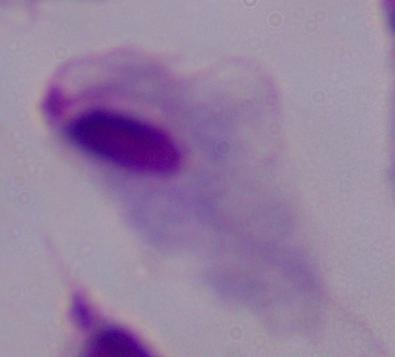

Summary:
  - Identification: trichomonad
  - Modality: micrograph
  - Magnification: 1000x